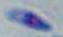
Toxoplasma gondii is seen. Photomicrograph. 1000x magnification.